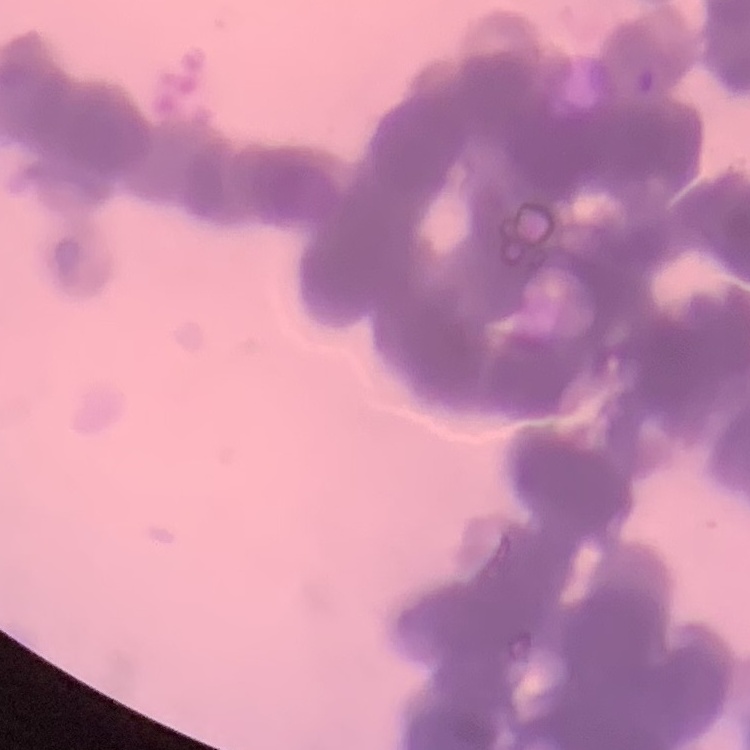 The erythrocytes show rouleaux formation. Field's or Giemsa stain. Square crop of a larger photomicrograph. Thin blood smear.